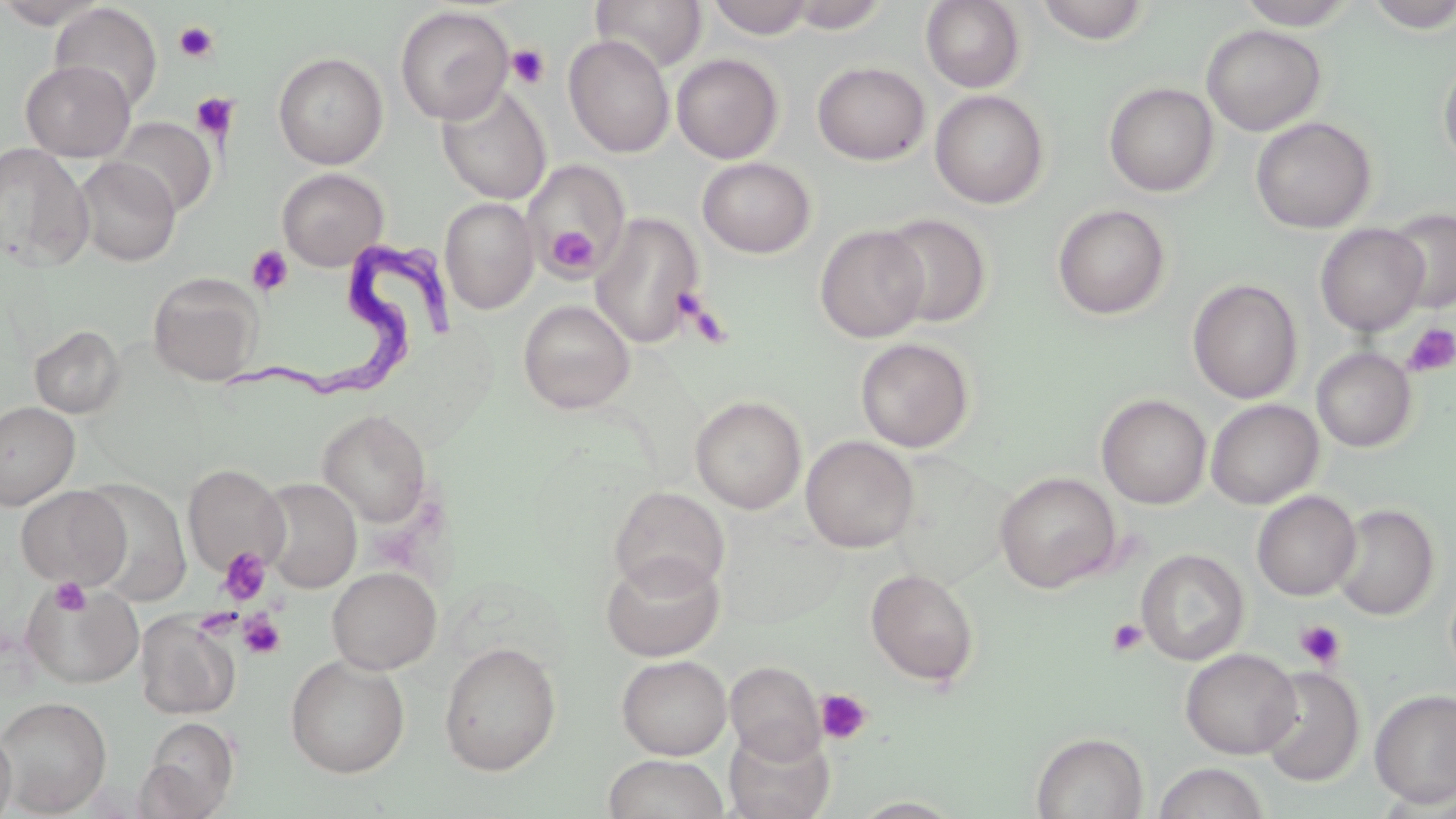
Summary:
  - Coordinate format: approximate bounding boxes as named x1/y1/x2/y2 corners in pixels
  - Trypanosoma brucei locations: (x1=233, y1=227, x2=456, y2=412)
  - Platelet locations: (x1=174, y1=21, x2=218, y2=62), (x1=506, y1=43, x2=550, y2=90), (x1=191, y1=93, x2=238, y2=138), (x1=546, y1=225, x2=599, y2=278), (x1=246, y1=245, x2=293, y2=297), (x1=674, y1=287, x2=721, y2=339), (x1=1403, y1=324, x2=1456, y2=378), (x1=217, y1=547, x2=272, y2=605), (x1=50, y1=577, x2=90, y2=615), (x1=193, y1=607, x2=242, y2=639), (x1=238, y1=611, x2=286, y2=659), (x1=1107, y1=618, x2=1148, y2=657), (x1=1295, y1=619, x2=1347, y2=670), (x1=815, y1=689, x2=872, y2=744)
  - Uninfected red blood cell locations: (x1=0, y1=0, x2=110, y2=29), (x1=591, y1=0, x2=706, y2=73), (x1=707, y1=0, x2=815, y2=39), (x1=784, y1=0, x2=891, y2=33), (x1=1033, y1=0, x2=1153, y2=44), (x1=1235, y1=0, x2=1359, y2=29), (x1=920, y1=1, x2=1026, y2=92), (x1=1362, y1=1, x2=1456, y2=32), (x1=49, y1=3, x2=163, y2=114), (x1=394, y1=5, x2=514, y2=124), (x1=1201, y1=24, x2=1326, y2=136), (x1=563, y1=34, x2=675, y2=158), (x1=273, y1=51, x2=388, y2=169), (x1=671, y1=54, x2=784, y2=163), (x1=1438, y1=54, x2=1456, y2=172), (x1=20, y1=59, x2=135, y2=161), (x1=812, y1=61, x2=930, y2=165), (x1=1103, y1=82, x2=1219, y2=197), (x1=437, y1=83, x2=552, y2=204), (x1=929, y1=89, x2=1050, y2=208), (x1=1251, y1=116, x2=1376, y2=234), (x1=110, y1=117, x2=216, y2=217), (x1=0, y1=142, x2=93, y2=273), (x1=74, y1=157, x2=180, y2=267), (x1=697, y1=157, x2=816, y2=258), (x1=522, y1=160, x2=631, y2=276), (x1=276, y1=168, x2=389, y2=270), (x1=440, y1=197, x2=539, y2=314), (x1=1052, y1=204, x2=1171, y2=320), (x1=1385, y1=208, x2=1456, y2=314), (x1=590, y1=212, x2=705, y2=349), (x1=879, y1=213, x2=992, y2=328), (x1=1315, y1=223, x2=1429, y2=336), (x1=815, y1=225, x2=930, y2=342), (x1=148, y1=273, x2=263, y2=386), (x1=1188, y1=278, x2=1303, y2=403), (x1=518, y1=299, x2=635, y2=414), (x1=30, y1=325, x2=125, y2=418), (x1=855, y1=337, x2=974, y2=452), (x1=1311, y1=347, x2=1416, y2=452), (x1=1096, y1=394, x2=1211, y2=509), (x1=690, y1=395, x2=807, y2=514), (x1=1205, y1=399, x2=1324, y2=509), (x1=0, y1=401, x2=79, y2=509), (x1=317, y1=409, x2=433, y2=527), (x1=801, y1=435, x2=919, y2=553), (x1=183, y1=464, x2=289, y2=577), (x1=995, y1=471, x2=1121, y2=593), (x1=257, y1=477, x2=361, y2=593), (x1=77, y1=479, x2=191, y2=605), (x1=15, y1=486, x2=130, y2=587), (x1=609, y1=486, x2=730, y2=596), (x1=1252, y1=490, x2=1361, y2=601), (x1=1332, y1=502, x2=1439, y2=621), (x1=715, y1=516, x2=848, y2=628), (x1=1136, y1=548, x2=1250, y2=665), (x1=601, y1=551, x2=724, y2=662), (x1=326, y1=566, x2=442, y2=675), (x1=865, y1=568, x2=980, y2=687), (x1=21, y1=580, x2=144, y2=690), (x1=135, y1=613, x2=239, y2=719), (x1=439, y1=641, x2=562, y2=775), (x1=1181, y1=648, x2=1301, y2=759), (x1=616, y1=654, x2=731, y2=760), (x1=285, y1=655, x2=411, y2=778), (x1=725, y1=661, x2=825, y2=763), (x1=1256, y1=666, x2=1365, y2=786), (x1=1369, y1=688, x2=1456, y2=808), (x1=0, y1=696, x2=112, y2=816), (x1=141, y1=717, x2=240, y2=815), (x1=0, y1=722, x2=16, y2=819), (x1=724, y1=723, x2=835, y2=819), (x1=1030, y1=731, x2=1148, y2=819), (x1=603, y1=754, x2=729, y2=819), (x1=1152, y1=762, x2=1271, y2=819), (x1=848, y1=796, x2=965, y2=818)
  - Slide-level diagnosis: Trypanosoma brucei
  - Preparation: thin blood smear
  - Field of view: one of a larger specimen
  - Modality: optical microscopy
  - Magnification: 1000x
  - Image size: 1456×819 pixels
  - Stain: May-Grünwald-Giemsa